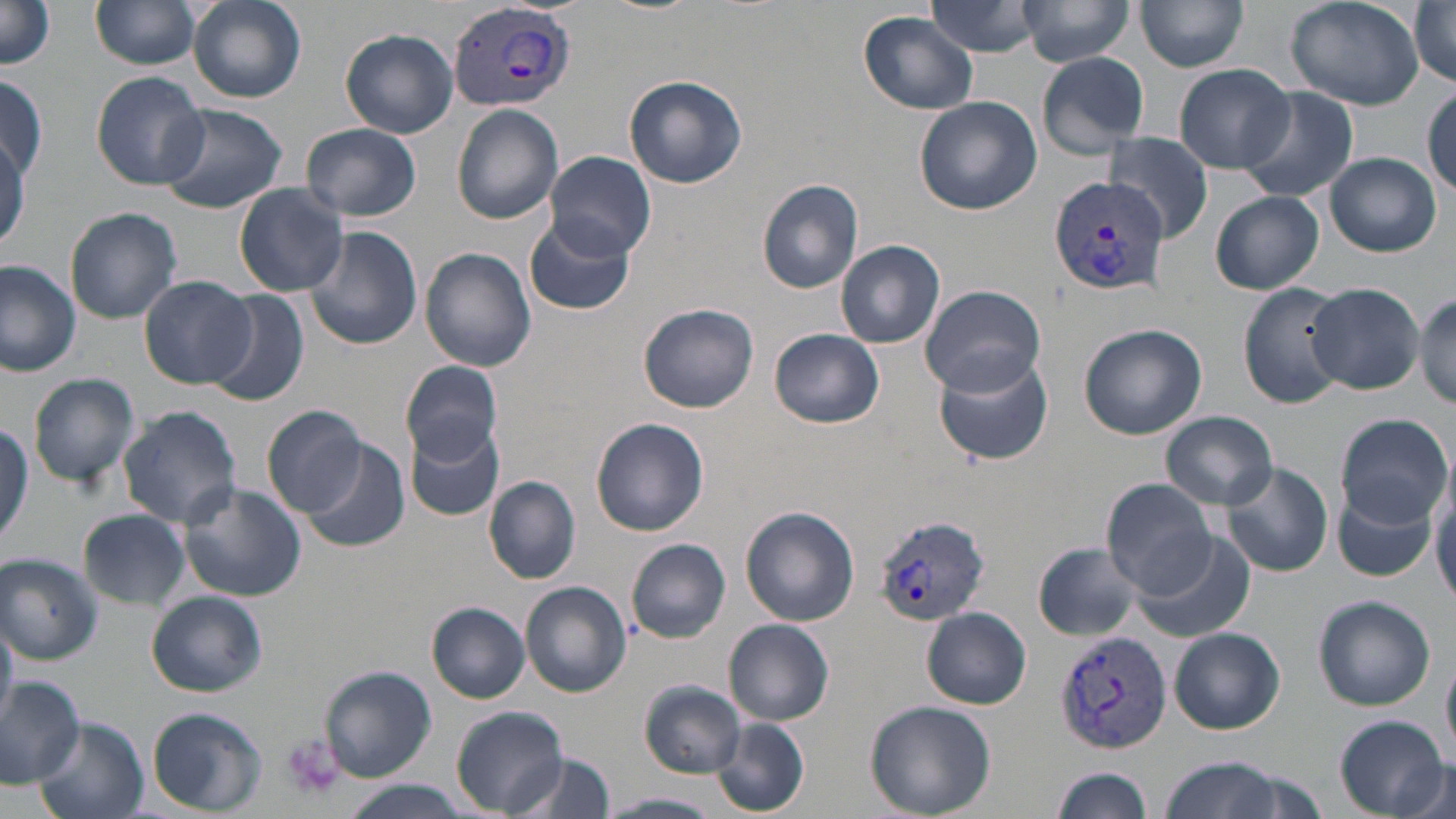
slide-level diagnosis = Plasmodium vivax
image size = 1456×819 pixels
modality = light microscopy
magnification = 1000x
field of view = one of a larger specimen
platelet locations = approximate bounding boxes as (x1,y1)-(x2,y2) corner pairs in pixels: (281,733)-(345,799)
stain = May-Grünwald-Giemsa
preparation = thin blood smear
Plasmodium vivax-infected red blood cell locations = approximate bounding boxes as (x1,y1)-(x2,y2) corner pairs in pixels: (445,1)-(578,113), (1047,178)-(1169,298), (872,513)-(991,625), (1054,629)-(1175,753)
uninfected red blood cell locations = approximate bounding boxes as (x1,y1)-(x2,y2) corner pairs in pixels: (187,0)-(307,103), (926,0)-(1044,58), (1019,0)-(1135,68), (1136,0)-(1250,72), (1283,0)-(1425,112), (1409,0)-(1456,88), (1,1)-(58,73), (91,2)-(202,70), (859,9)-(981,116), (340,27)-(461,138), (1036,50)-(1150,158), (1173,63)-(1295,173), (91,71)-(210,188), (624,73)-(747,189), (0,78)-(48,183), (1424,84)-(1456,197), (1236,86)-(1358,204), (914,95)-(1042,214), (155,104)-(288,214), (452,104)-(563,225), (300,122)-(423,221), (0,128)-(27,252), (1104,134)-(1213,244), (547,150)-(656,260), (1326,152)-(1441,255), (756,178)-(865,294), (233,183)-(349,297), (1210,192)-(1324,295), (65,207)-(183,323), (525,216)-(634,316), (303,225)-(423,351), (836,240)-(946,350), (420,248)-(537,371), (0,261)-(80,377), (140,275)-(256,388), (1238,281)-(1351,410), (1306,283)-(1424,393), (919,285)-(1045,396), (204,289)-(311,407), (1413,293)-(1455,409), (639,303)-(762,414), (1077,322)-(1206,440), (771,329)-(883,428), (930,353)-(1055,469), (401,360)-(503,465), (27,372)-(140,490), (263,404)-(371,518), (118,406)-(243,529), (1162,411)-(1278,508), (1335,411)-(1452,528), (591,417)-(709,537), (0,419)-(31,553), (403,421)-(505,522), (299,438)-(408,551), (1224,461)-(1333,575), (1430,468)-(1456,603), (485,477)-(580,584), (1101,479)-(1217,597), (1332,483)-(1440,583), (180,484)-(303,602), (740,506)-(860,627), (79,510)-(191,610), (1129,530)-(1259,644), (625,539)-(731,644), (1031,546)-(1142,639), (0,553)-(102,665), (520,581)-(631,697), (148,592)-(266,696), (1313,595)-(1436,711), (427,602)-(531,703), (922,608)-(1031,709), (724,618)-(835,726), (0,619)-(16,728), (1170,627)-(1285,734), (1442,649)-(1456,767), (320,665)-(436,782), (0,678)-(86,786), (640,681)-(745,776), (865,701)-(996,818), (147,707)-(267,816), (451,707)-(569,817), (1334,715)-(1449,815), (33,717)-(145,819), (712,718)-(809,815), (517,754)-(616,818), (1160,756)-(1288,819), (1394,758)-(1453,817), (1050,767)-(1155,818), (338,781)-(471,818), (603,792)-(722,818)